State the preparation type.
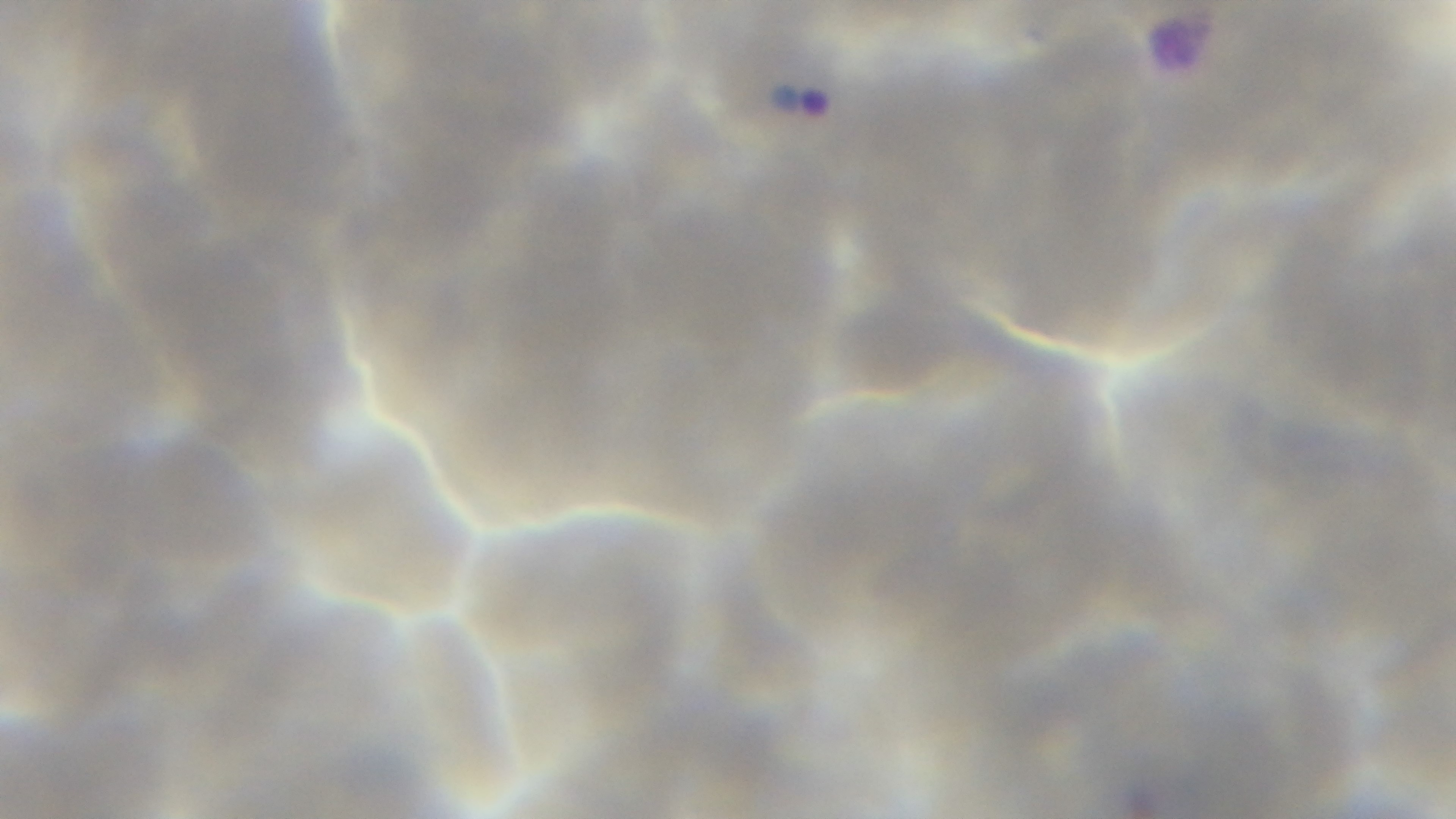
Thin.

stain = Giemsa
field of view = one from the slide
modality = light microscopy
objective = 100x oil immersion
capture = mounted 4K digital camera
malaria status = infected